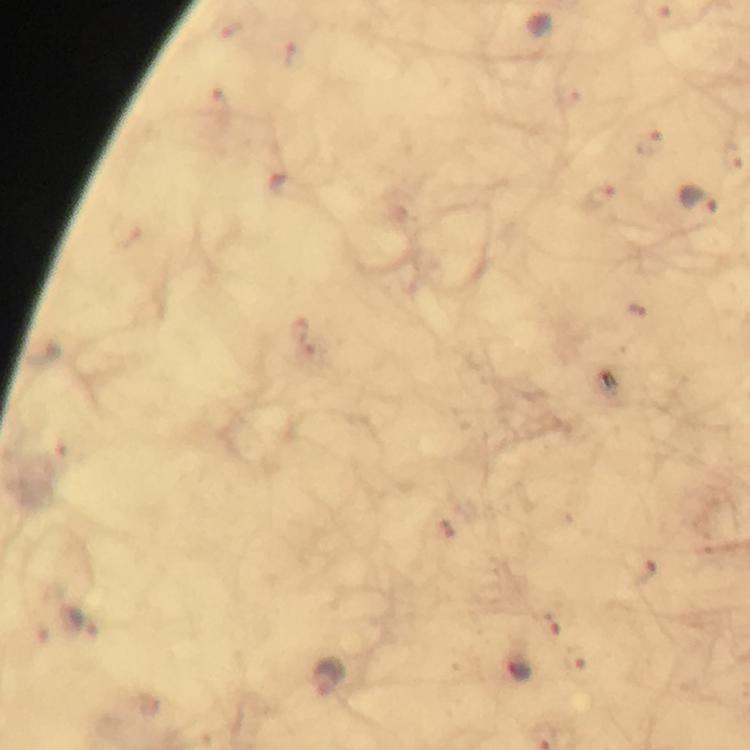
capture = smartphone camera through the microscope
image size = 750×750 pixels
stain = Giemsa
malaria parasite locations = approximate centers as {x, y} in pixels: {649, 142}, {606, 198}, {700, 199}, {552, 622}, {522, 668}, {331, 680}
magnification = 100x
cropped from = one field of view
context = from a malaria diagnostic workup
preparation = thick smear
immersion oil = used